Mark where leukocytes are.
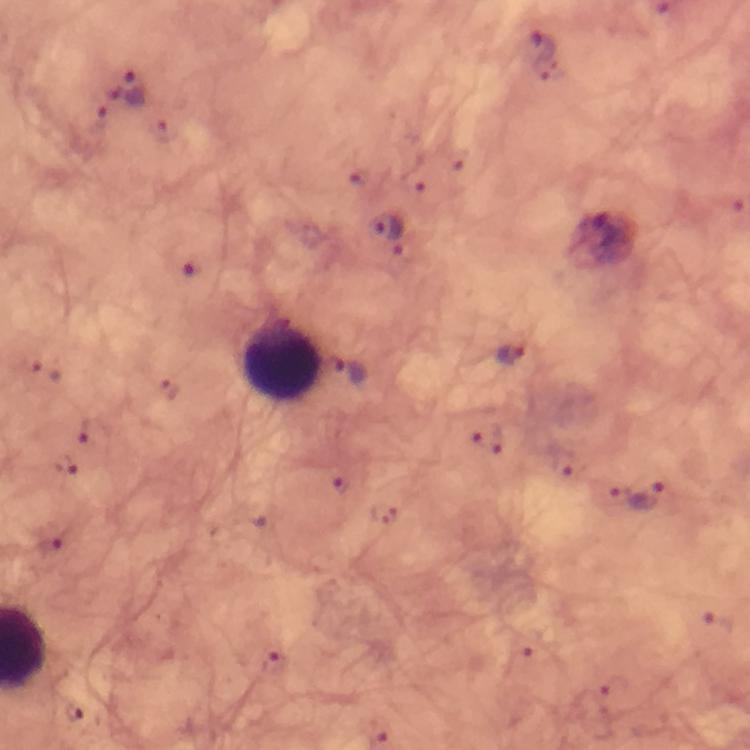

Approximate centers as {x, y} in pixels.
Leukocytes: {282, 358}.

Summary:
  - Plasmodium parasite locations: {540, 48}, {128, 91}, {388, 228}, {509, 356}, {350, 374}, {648, 496}, {52, 550}, {721, 624}, {519, 659}, {273, 661}, {612, 689}, {76, 714}
  - Immersion oil: used
  - Context: from a malaria diagnostic workup
  - Preparation: thick blood smear
  - Cropped from: a single field of view
  - Magnification: 100x
  - Capture: smartphone photograph through a microscope
  - Image size: 750×750 pixels
  - Stain: Giemsa